Give the extent of all Plasmodium ovale-infected red blood cells.
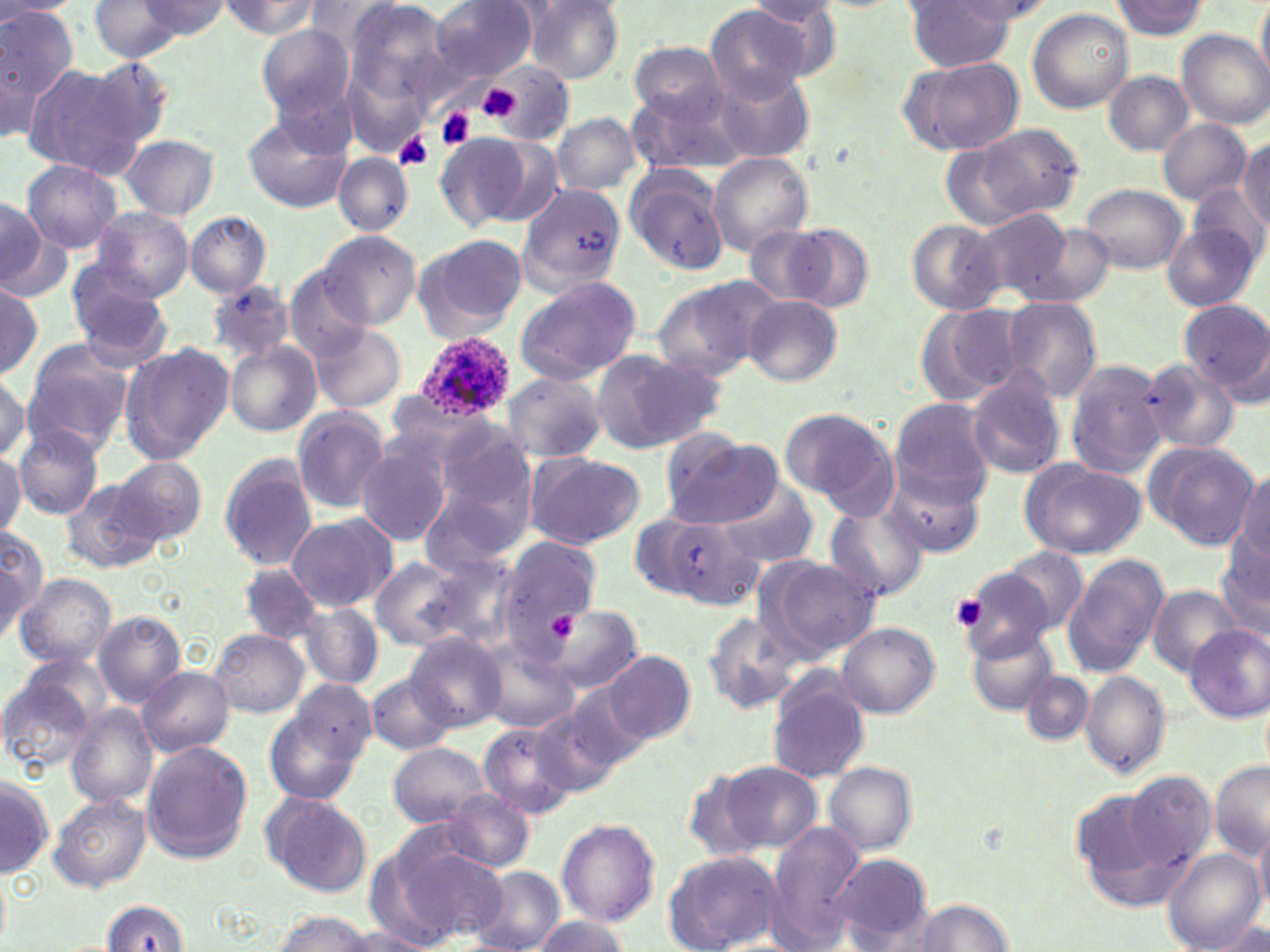
Approximate bounding boxes as (x1, y1, x2, y2) in pixels.
Plasmodium ovale-infected red blood cells: (413, 331, 517, 422).

Platelet locations: (477, 84, 525, 124), (437, 108, 475, 148), (393, 131, 435, 171), (952, 595, 990, 631). Uninfected red blood cell locations: (0, 0, 77, 133), (89, 0, 195, 63), (216, 0, 325, 38), (342, 0, 457, 107), (432, 0, 538, 84), (1256, 0, 1270, 86), (0, 1, 83, 20), (135, 1, 232, 38), (522, 1, 626, 83), (905, 1, 1017, 71), (1109, 1, 1210, 39), (705, 4, 811, 106), (1028, 8, 1133, 112), (257, 25, 355, 121), (1177, 29, 1269, 129), (630, 41, 726, 119), (900, 53, 1022, 156), (81, 55, 176, 159), (20, 61, 141, 179), (470, 68, 574, 138), (713, 70, 817, 165), (1104, 70, 1194, 155), (628, 85, 750, 176), (241, 111, 351, 213), (550, 113, 643, 195), (1158, 119, 1252, 206), (959, 122, 1084, 225), (436, 133, 529, 227), (120, 134, 218, 220), (480, 135, 566, 228), (1240, 135, 1270, 229), (937, 139, 1038, 229), (333, 153, 412, 236), (706, 153, 813, 255), (23, 159, 123, 255), (624, 165, 729, 274), (517, 181, 629, 290), (1081, 183, 1187, 274), (1191, 185, 1267, 267), (0, 197, 53, 299), (92, 207, 194, 300), (971, 210, 1074, 303), (185, 211, 271, 297), (907, 220, 1006, 315), (1014, 221, 1114, 309), (784, 222, 874, 313), (746, 224, 837, 306), (1163, 224, 1260, 311), (318, 229, 421, 329), (419, 234, 528, 336), (67, 259, 171, 359), (282, 269, 376, 360), (513, 275, 643, 384), (654, 276, 782, 378), (209, 280, 294, 364), (0, 282, 43, 381), (743, 295, 840, 386), (1002, 297, 1102, 402), (1182, 300, 1270, 400), (914, 304, 1026, 408), (309, 323, 406, 414), (22, 340, 134, 455), (226, 340, 323, 437), (120, 344, 233, 464), (589, 349, 721, 453), (1137, 358, 1240, 456), (1065, 359, 1171, 478), (965, 368, 1066, 480), (0, 372, 29, 463), (501, 373, 607, 461), (891, 399, 994, 498), (291, 407, 390, 513), (780, 408, 891, 504), (14, 425, 103, 518), (419, 426, 541, 559), (661, 433, 782, 529), (355, 439, 454, 547), (1145, 442, 1259, 551), (0, 448, 25, 539), (521, 451, 645, 550), (218, 455, 318, 571), (112, 456, 207, 545), (1020, 458, 1147, 559), (884, 462, 987, 557), (1235, 469, 1269, 562), (60, 477, 167, 575), (232, 480, 360, 596), (714, 484, 821, 567), (825, 502, 930, 601), (642, 510, 762, 612), (285, 513, 397, 612), (0, 525, 46, 636), (1216, 531, 1270, 640), (499, 534, 601, 644), (999, 549, 1090, 636), (414, 552, 521, 650), (1062, 554, 1169, 678), (370, 555, 479, 654), (757, 555, 880, 661), (956, 560, 1060, 659), (240, 565, 325, 644), (16, 573, 117, 669), (1148, 586, 1241, 674), (299, 601, 382, 690), (546, 605, 641, 693), (94, 610, 187, 707), (701, 611, 799, 713), (837, 622, 939, 718), (1185, 624, 1270, 722), (209, 628, 311, 718), (969, 631, 1056, 716), (406, 632, 506, 731), (477, 636, 581, 733), (604, 651, 695, 744), (15, 652, 116, 738), (138, 665, 234, 756), (0, 668, 100, 775), (1022, 670, 1094, 745), (1080, 671, 1170, 776), (367, 672, 456, 755), (767, 672, 869, 784), (287, 678, 377, 773), (555, 685, 650, 779), (264, 700, 368, 804), (66, 704, 159, 806), (535, 706, 623, 800), (477, 721, 579, 819), (140, 741, 252, 864), (389, 742, 490, 827), (718, 760, 822, 855), (1209, 760, 1269, 861), (824, 761, 917, 856), (1122, 770, 1217, 872), (1, 779, 52, 877), (263, 791, 374, 898), (438, 791, 534, 872), (51, 794, 152, 893), (557, 819, 659, 927), (766, 822, 865, 948), (1254, 825, 1270, 920), (392, 844, 510, 943), (1162, 847, 1266, 952), (663, 850, 783, 951), (362, 854, 463, 951), (828, 854, 934, 949), (472, 866, 566, 952), (0, 870, 11, 946), (909, 899, 1013, 952), (102, 900, 192, 951), (268, 910, 382, 952), (533, 914, 629, 952), (339, 929, 437, 951). Slide-level diagnosis: Plasmodium ovale. Single field of view. Thin blood smear. Captured at 1000x magnification. Light microscopy. Image is 1270×952 pixels. May-Grünwald-Giemsa stain.